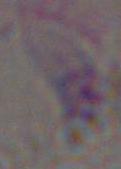

Summary:
  - Identification: Toxoplasma gondii
  - Modality: photomicrograph
  - Magnification: 1000x